Report the malaria status of this cell.
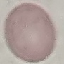
It is uninfected.

Cell patch, automatically extracted from a larger field of view and resized to 64 × 64 pixels. Photographed with a smartphone camera at the microscope eyepiece. Giemsa-stained preparation. Thin smear of blood.